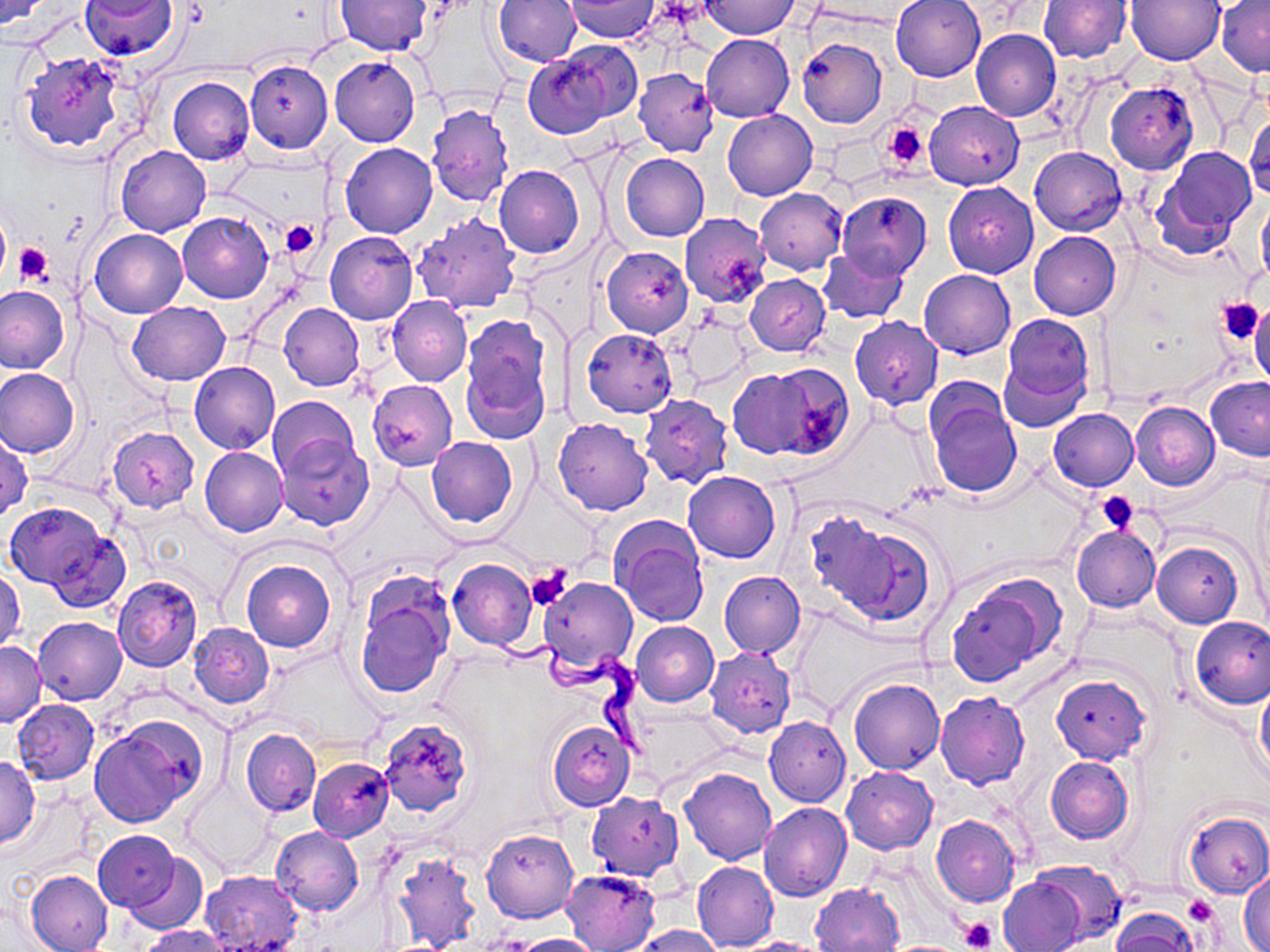
Summary:
  - Coordinate format: approximate bounding boxes as (x1, y1, x2, y2) in pixels
  - Uninfected red blood cell locations: (0, 0, 53, 28), (80, 0, 178, 61), (565, 0, 659, 42), (891, 0, 986, 81), (1125, 0, 1224, 65), (1216, 0, 1270, 75), (335, 1, 434, 56), (493, 1, 580, 68), (699, 1, 800, 39), (1039, 1, 1130, 63), (972, 30, 1061, 121), (701, 34, 795, 122), (797, 38, 886, 128), (546, 40, 644, 127), (20, 51, 125, 152), (523, 54, 613, 137), (330, 56, 421, 146), (245, 60, 333, 152), (634, 67, 718, 156), (168, 77, 254, 165), (1106, 83, 1198, 173), (925, 101, 1024, 190), (426, 105, 513, 207), (722, 110, 817, 200), (1245, 114, 1270, 202), (340, 143, 437, 238), (114, 145, 211, 236), (1154, 147, 1256, 250), (1030, 148, 1127, 236), (620, 153, 709, 241), (495, 165, 584, 258), (943, 181, 1038, 278), (754, 187, 847, 275), (837, 191, 932, 279), (1258, 197, 1270, 287), (178, 212, 273, 304), (411, 212, 521, 314), (678, 212, 770, 307), (89, 229, 188, 317), (324, 231, 417, 325), (1030, 231, 1121, 319), (601, 247, 693, 337), (817, 247, 908, 323), (918, 269, 1015, 359), (744, 273, 830, 355), (0, 284, 69, 373), (388, 296, 472, 386), (127, 301, 231, 385), (1249, 302, 1270, 389), (279, 303, 364, 390), (1001, 312, 1094, 423), (460, 314, 552, 440), (677, 314, 752, 389), (850, 316, 942, 408), (580, 327, 678, 417), (189, 362, 280, 454), (726, 364, 842, 461), (0, 368, 79, 458), (1205, 376, 1270, 460), (367, 379, 457, 470), (927, 388, 1022, 502), (640, 395, 734, 489), (267, 396, 358, 479), (1131, 402, 1218, 490), (1048, 408, 1138, 490), (553, 419, 652, 515), (108, 427, 199, 511), (275, 432, 375, 531), (1, 433, 32, 522), (427, 436, 518, 527), (200, 446, 288, 536), (684, 471, 780, 563), (5, 502, 107, 589), (811, 515, 931, 625), (613, 522, 708, 627), (1070, 525, 1160, 611), (49, 529, 131, 613), (1151, 541, 1242, 628), (241, 559, 335, 653), (447, 559, 537, 650), (1, 568, 25, 654), (719, 571, 805, 657), (943, 571, 1066, 688), (113, 575, 203, 672), (352, 576, 454, 699), (539, 576, 637, 672), (1190, 616, 1270, 708), (34, 617, 127, 705), (631, 621, 719, 706), (188, 622, 274, 708), (0, 641, 46, 727), (705, 647, 796, 738), (1051, 672, 1151, 764), (849, 678, 945, 774), (1255, 678, 1270, 783), (935, 692, 1029, 789), (14, 700, 99, 783), (764, 717, 850, 806), (377, 718, 472, 816), (90, 719, 204, 826), (547, 720, 635, 811), (242, 729, 320, 816), (0, 754, 41, 847), (1046, 756, 1134, 843), (309, 758, 393, 841), (841, 766, 937, 853), (679, 767, 776, 865), (186, 780, 273, 871), (586, 792, 684, 881), (573, 796, 675, 950), (760, 803, 851, 902), (1182, 810, 1270, 898), (931, 815, 1020, 908), (271, 827, 363, 914), (93, 829, 181, 913), (481, 829, 577, 924), (389, 849, 481, 951), (123, 852, 207, 934), (692, 860, 778, 952), (1028, 861, 1127, 945), (563, 868, 661, 951), (24, 869, 113, 951), (198, 869, 301, 952), (1239, 870, 1270, 952), (998, 877, 1085, 952), (810, 882, 904, 952), (1110, 909, 1200, 952), (632, 924, 726, 951), (139, 925, 232, 952), (500, 932, 603, 952), (730, 936, 835, 952)
  - Platelet locations: (881, 119, 931, 172), (279, 219, 320, 257), (0, 221, 12, 282), (14, 244, 52, 287), (1217, 297, 1267, 344), (1096, 491, 1139, 535), (526, 566, 573, 611), (1183, 894, 1218, 924), (962, 916, 997, 950)
  - Trypanosoma brucei locations: (486, 630, 648, 755)
  - Slide-level diagnosis: Trypanosoma brucei
  - Modality: optical microscopy
  - Stain: May-Grünwald-Giemsa
  - Preparation: thin blood film
  - Field of view: one of a larger specimen
  - Image size: 1270×952 pixels
  - Magnification: 1000x